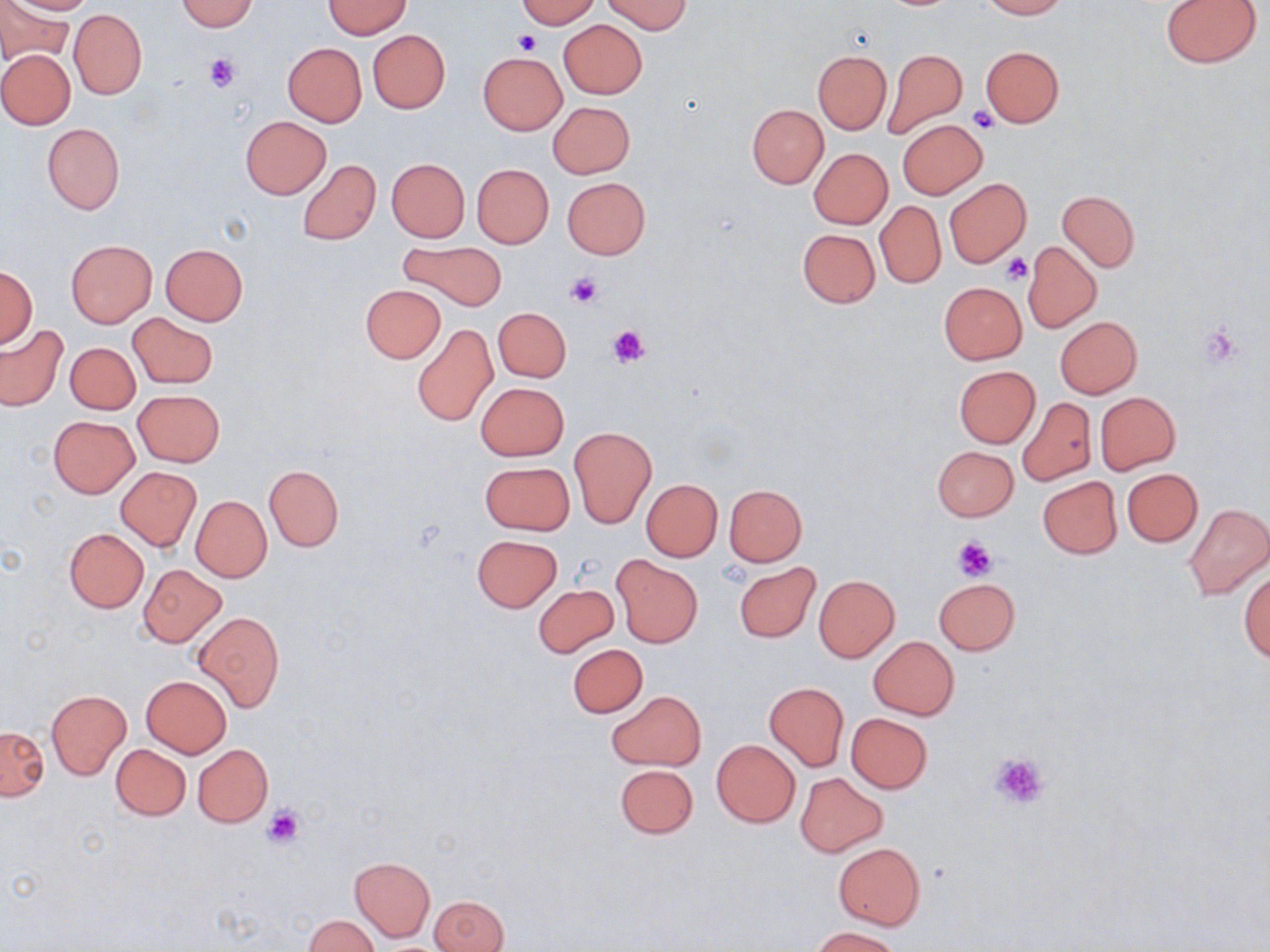
Approximate bounding boxes as [x1, y1, x2, y2] in pixels. Uninfected red blood cell locations: [6, 0, 98, 14], [175, 0, 260, 32], [323, 0, 412, 38], [516, 0, 600, 27], [978, 0, 1066, 19], [604, 1, 692, 34], [1161, 1, 1262, 67], [0, 2, 73, 61], [69, 8, 147, 99], [558, 19, 649, 99], [368, 30, 451, 113], [282, 42, 366, 126], [979, 45, 1065, 127], [0, 50, 75, 129], [883, 50, 966, 138], [813, 52, 891, 133], [478, 53, 567, 134], [548, 102, 635, 178], [748, 104, 827, 188], [240, 115, 331, 197], [897, 119, 988, 199], [43, 123, 125, 214], [809, 148, 893, 229], [385, 158, 470, 243], [296, 159, 381, 246], [472, 164, 553, 248], [563, 177, 649, 259], [945, 178, 1031, 267], [1058, 190, 1140, 270], [875, 200, 946, 288], [797, 228, 880, 308], [66, 240, 157, 327], [400, 241, 506, 311], [1023, 242, 1102, 332], [160, 244, 248, 325], [1, 266, 37, 348], [938, 281, 1027, 364], [359, 284, 446, 362], [492, 307, 571, 382], [127, 312, 218, 387], [1054, 316, 1142, 397], [412, 323, 496, 426], [0, 325, 68, 412], [65, 343, 140, 414], [953, 365, 1040, 448], [475, 382, 569, 461], [133, 390, 225, 467], [1095, 392, 1181, 474], [1018, 398, 1096, 487], [48, 416, 139, 497], [569, 427, 656, 527], [931, 445, 1019, 521], [480, 461, 574, 535], [115, 466, 202, 551], [265, 466, 344, 550], [1122, 468, 1203, 546], [1038, 477, 1122, 558], [641, 479, 723, 561], [725, 484, 806, 566], [191, 496, 271, 581], [1183, 502, 1270, 600], [64, 529, 148, 612], [473, 534, 561, 611], [614, 556, 702, 647], [734, 563, 820, 641], [137, 564, 227, 645], [1239, 564, 1270, 663], [814, 576, 899, 661], [934, 577, 1021, 655], [533, 584, 618, 657], [194, 609, 284, 711], [869, 636, 959, 719], [567, 644, 647, 718], [141, 675, 232, 757], [764, 683, 848, 770], [47, 690, 131, 778], [608, 691, 706, 769], [846, 713, 933, 793], [1, 725, 48, 800], [712, 739, 800, 828], [111, 744, 191, 819], [193, 744, 273, 826], [614, 763, 698, 839], [795, 771, 889, 857], [833, 841, 925, 929], [350, 857, 435, 942], [430, 895, 508, 952], [306, 915, 378, 951], [810, 927, 903, 952]. Platelet locations: [514, 29, 540, 56], [204, 54, 241, 93], [968, 107, 1000, 132], [1001, 252, 1032, 284], [564, 271, 605, 308], [610, 324, 649, 366], [1201, 324, 1242, 367], [952, 537, 996, 581], [988, 752, 1049, 810], [261, 805, 305, 850]. Slide-level diagnosis: negative for blood parasites. Light microscopy. Image is 1270×952 pixels. May-Grünwald-Giemsa stain. Thin blood smear. Single field of view. 1000x magnification.